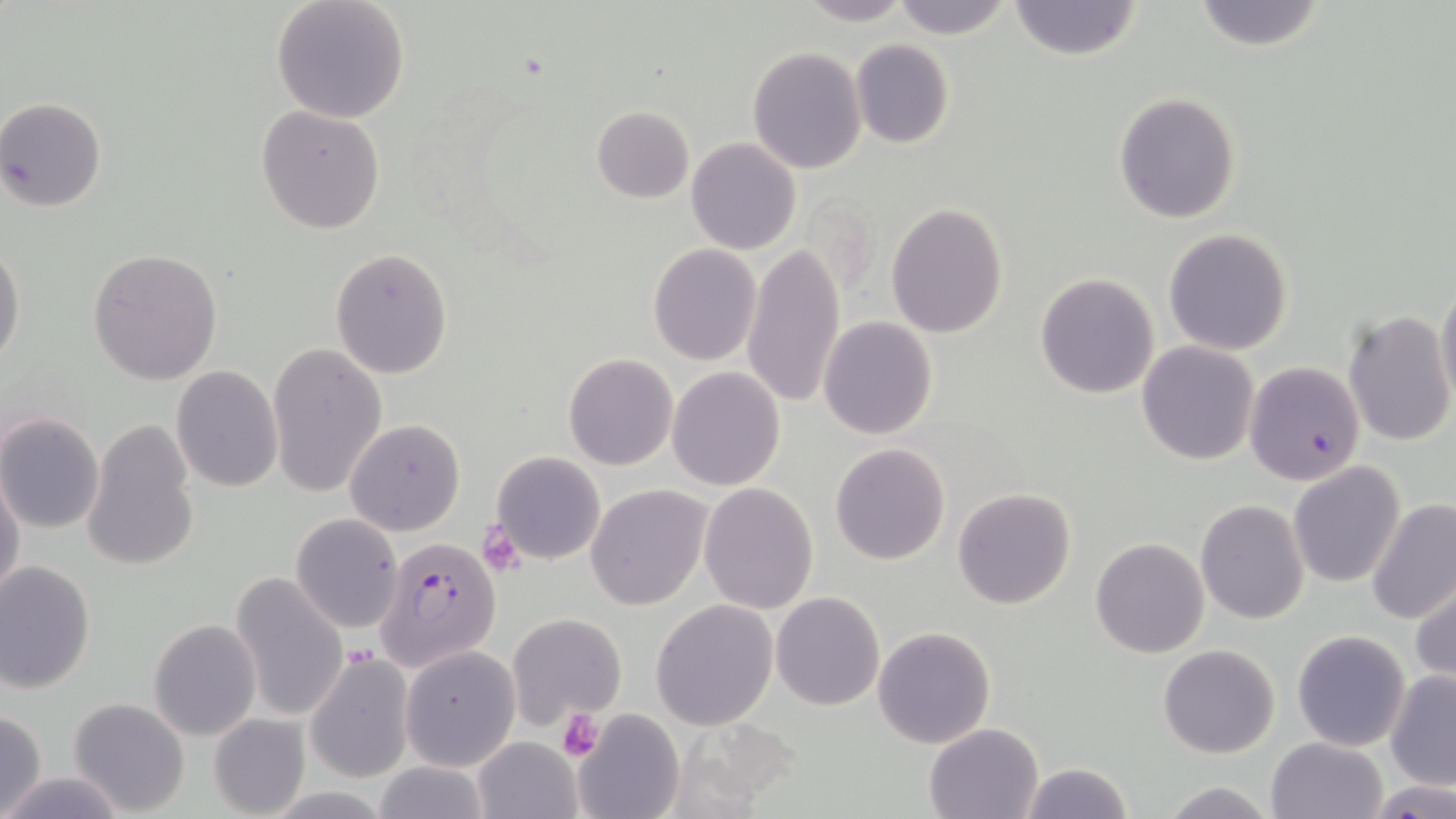

Approximate bounding boxes as named x1/y1/x2/y2 corners in pixels. Platelet locations: (x1=555, y1=709, x2=604, y2=761). Plasmodium falciparum-infected red blood cell locations: (x1=1243, y1=361, x2=1365, y2=486), (x1=373, y1=535, x2=501, y2=674). Uninfected red blood cell locations: (x1=270, y1=0, x2=410, y2=123), (x1=793, y1=0, x2=916, y2=25), (x1=889, y1=0, x2=1014, y2=40), (x1=1007, y1=0, x2=1143, y2=60), (x1=1188, y1=0, x2=1330, y2=52), (x1=850, y1=39, x2=955, y2=149), (x1=747, y1=48, x2=867, y2=174), (x1=1113, y1=92, x2=1241, y2=223), (x1=1, y1=98, x2=107, y2=210), (x1=590, y1=105, x2=692, y2=204), (x1=255, y1=106, x2=386, y2=233), (x1=685, y1=137, x2=801, y2=254), (x1=886, y1=202, x2=1008, y2=338), (x1=1162, y1=228, x2=1294, y2=356), (x1=0, y1=243, x2=25, y2=369), (x1=647, y1=244, x2=762, y2=366), (x1=741, y1=244, x2=847, y2=409), (x1=87, y1=248, x2=223, y2=385), (x1=330, y1=249, x2=454, y2=378), (x1=1035, y1=272, x2=1160, y2=399), (x1=1434, y1=275, x2=1456, y2=412), (x1=1341, y1=309, x2=1454, y2=447), (x1=818, y1=317, x2=938, y2=440), (x1=266, y1=340, x2=386, y2=499), (x1=1136, y1=340, x2=1259, y2=466), (x1=564, y1=353, x2=678, y2=471), (x1=170, y1=366, x2=283, y2=494), (x1=666, y1=367, x2=786, y2=491), (x1=0, y1=412, x2=105, y2=534), (x1=345, y1=418, x2=466, y2=535), (x1=81, y1=420, x2=201, y2=572), (x1=829, y1=443, x2=949, y2=566), (x1=491, y1=451, x2=606, y2=566), (x1=1287, y1=461, x2=1406, y2=588), (x1=0, y1=468, x2=25, y2=605), (x1=699, y1=483, x2=820, y2=613), (x1=586, y1=484, x2=712, y2=610), (x1=951, y1=486, x2=1076, y2=611), (x1=1365, y1=499, x2=1455, y2=629), (x1=1194, y1=500, x2=1309, y2=625), (x1=290, y1=513, x2=403, y2=634), (x1=1090, y1=536, x2=1211, y2=658), (x1=0, y1=559, x2=96, y2=695), (x1=228, y1=572, x2=351, y2=723), (x1=1410, y1=577, x2=1456, y2=690), (x1=772, y1=592, x2=886, y2=711), (x1=651, y1=599, x2=778, y2=730), (x1=506, y1=613, x2=627, y2=726), (x1=148, y1=618, x2=261, y2=739), (x1=872, y1=626, x2=997, y2=749), (x1=1292, y1=629, x2=1411, y2=751), (x1=1158, y1=643, x2=1279, y2=758), (x1=401, y1=646, x2=520, y2=771), (x1=303, y1=652, x2=415, y2=784), (x1=1385, y1=670, x2=1456, y2=791), (x1=68, y1=697, x2=191, y2=817), (x1=572, y1=706, x2=685, y2=819), (x1=0, y1=707, x2=47, y2=819), (x1=209, y1=712, x2=312, y2=816), (x1=924, y1=722, x2=1044, y2=819), (x1=472, y1=736, x2=581, y2=818), (x1=1266, y1=737, x2=1388, y2=819), (x1=1018, y1=760, x2=1133, y2=818), (x1=369, y1=761, x2=493, y2=818), (x1=1, y1=770, x2=124, y2=818), (x1=1157, y1=779, x2=1278, y2=819), (x1=1372, y1=781, x2=1454, y2=817). Slide-level diagnosis: Plasmodium falciparum. Thin blood film. Optical microscopy. Image is 1456×819 pixels. Single field of view. May-Grünwald-Giemsa-stained preparation. Captured at 1000x magnification.